State which cell type is depicted.
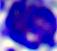

A leukocyte.

400x magnification. Photomicrograph.